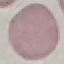

Malaria status: uninfected. Thin smear of blood. Automatically extracted cell patch, resized to 64 × 64 pixels. Giemsa stain. Photographed with a smartphone camera at the microscope eyepiece.